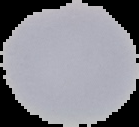

Result: no malaria parasites seen. Image is 139×127 pixels. The area outside the segmented cell region is set to black. From a thin blood film.